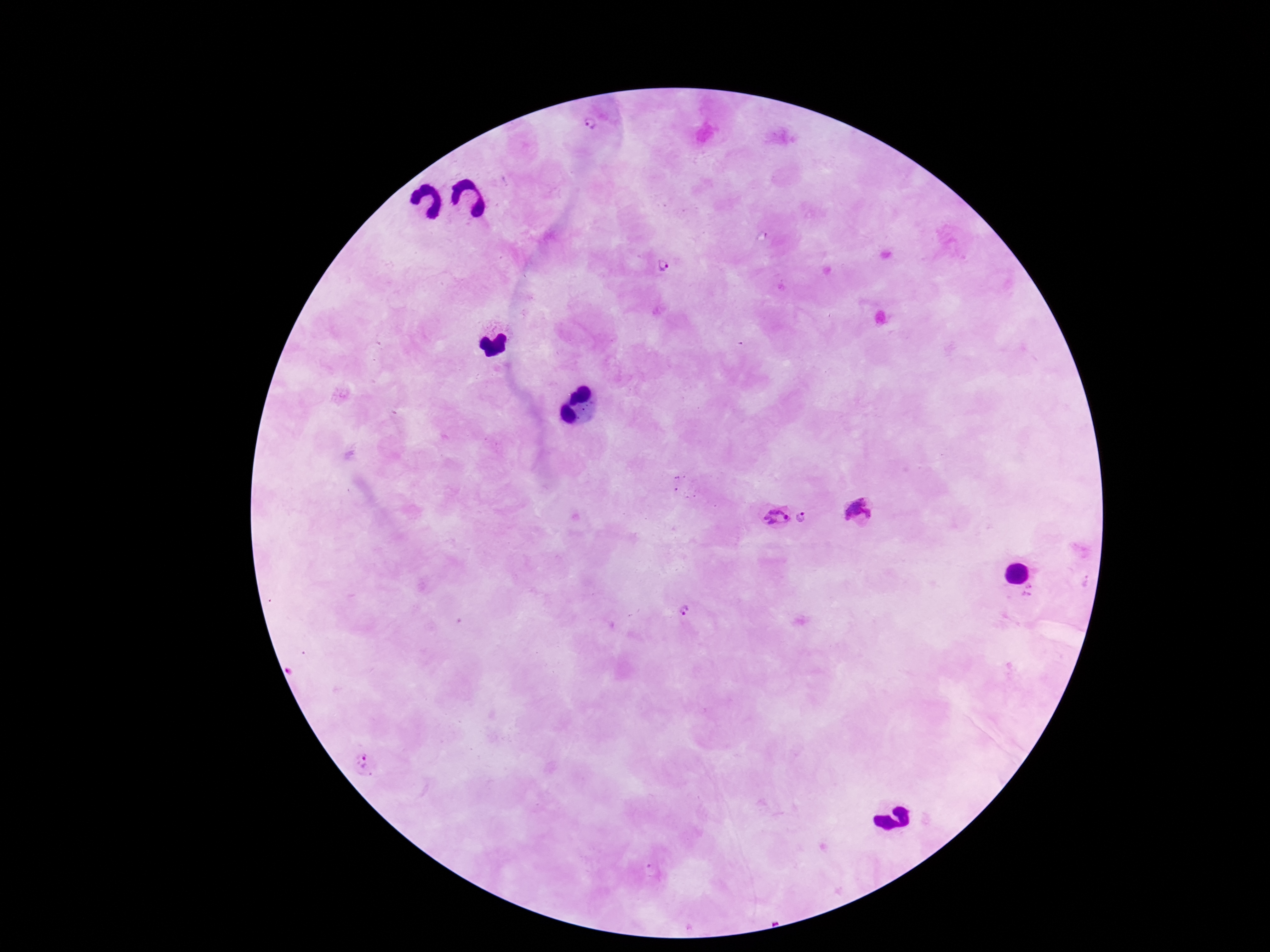
Approximate centers as {x, y} in pixels. Plasmodium parasite locations: {591, 126}, {662, 267}, {859, 511}, {774, 517}, {807, 518}, {1085, 581}, {1029, 591}, {684, 610}, {365, 762}. Image is 1270×952 pixels. 100x magnification. Giemsa-stained preparation. Single field of view. Smartphone photograph taken through the microscope eyepiece. Patient malaria status: infected. Thick blood smear.